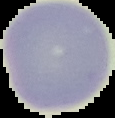

Summary:
  - Image size: 115×118 pixels
  - Image type: segmented cell region on a black background
  - Result: no malaria parasites seen
  - Preparation: thin blood smear